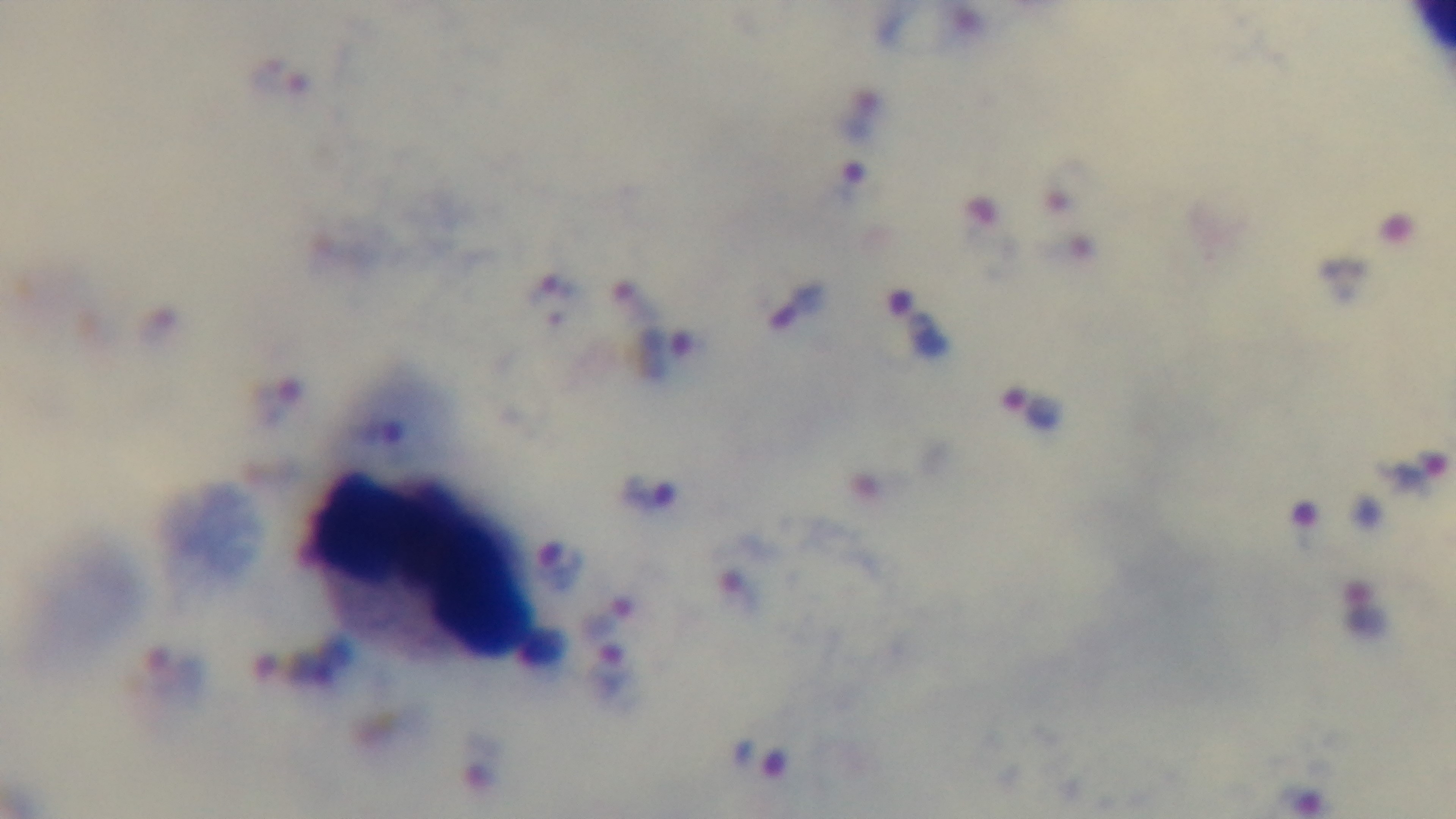
Summary:
  - Modality: light microscopy
  - Field of view: one from the slide
  - Stain: Giemsa
  - Objective: 100x oil immersion
  - Malaria status: positive
  - Capture: mounted 4K digital camera
  - Preparation: thick smear